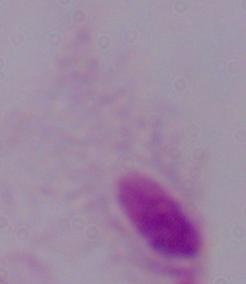 A trichomonad is seen. Captured at 1000x magnification. Photomicrograph.